Identify the parasite.
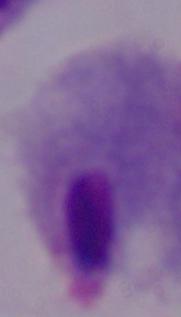
A trichomonad.

Summary:
  - Magnification: 1000x
  - Modality: photomicrograph